Assess the morphology of the red blood cells.
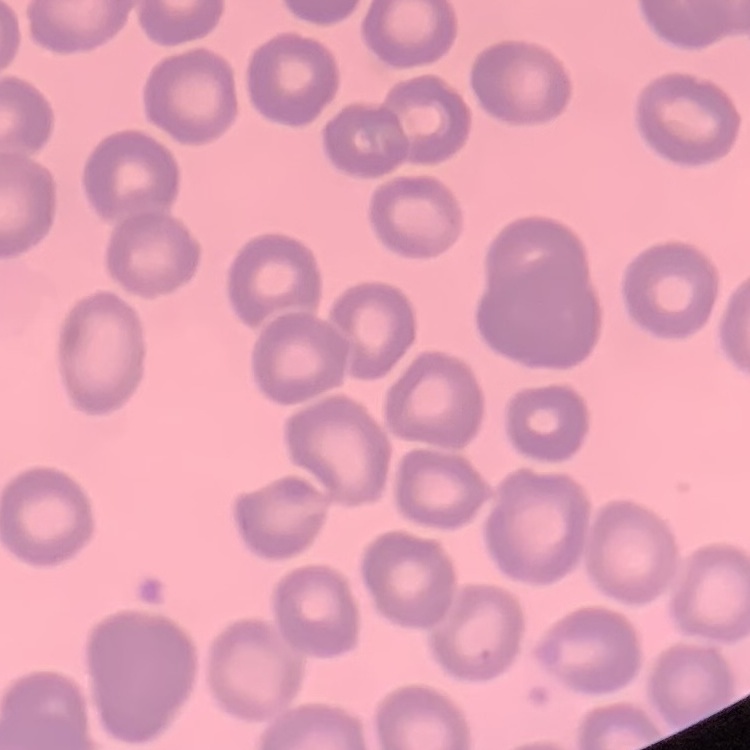
No rouleaux formation.

Thin blood film. Square crop of a larger photomicrograph. Field's or Giemsa stain.